Locate every Trypanosoma brucei.
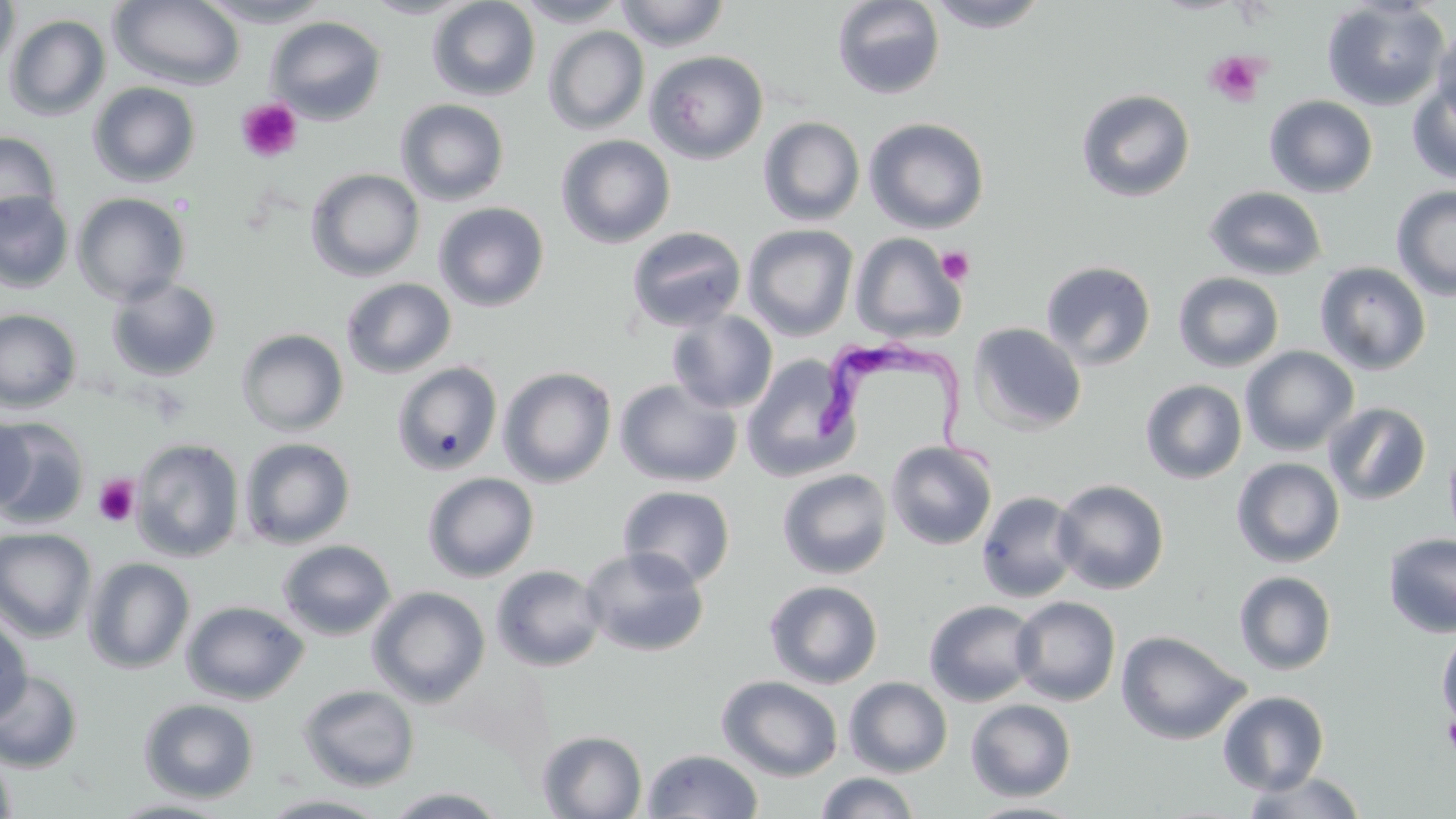
Approximate bounding boxes as named x1/y1/x2/y2 corners in pixels.
Trypanosoma brucei: (x1=814, y1=330, x2=1003, y2=482).

slide-level diagnosis = Trypanosoma brucei
field of view = single
platelet locations = approximate bounding boxes as named x1/y1/x2/y2 corners in pixels: (x1=1204, y1=51, x2=1267, y2=108), (x1=236, y1=98, x2=303, y2=163), (x1=936, y1=246, x2=975, y2=286), (x1=93, y1=474, x2=141, y2=527), (x1=1441, y1=715, x2=1456, y2=758)
uninfected red blood cell locations = approximate bounding boxes as named x1/y1/x2/y2 corners in pixels: (x1=0, y1=0, x2=20, y2=75), (x1=109, y1=0, x2=247, y2=91), (x1=193, y1=0, x2=334, y2=27), (x1=360, y1=0, x2=478, y2=19), (x1=427, y1=0, x2=541, y2=102), (x1=513, y1=0, x2=630, y2=27), (x1=614, y1=0, x2=730, y2=51), (x1=831, y1=0, x2=946, y2=100), (x1=925, y1=0, x2=1052, y2=33), (x1=1321, y1=1, x2=1450, y2=111), (x1=5, y1=14, x2=110, y2=122), (x1=265, y1=16, x2=387, y2=125), (x1=1432, y1=20, x2=1456, y2=128), (x1=543, y1=26, x2=649, y2=135), (x1=645, y1=51, x2=769, y2=165), (x1=1406, y1=80, x2=1456, y2=185), (x1=88, y1=82, x2=201, y2=187), (x1=1075, y1=88, x2=1195, y2=203), (x1=1264, y1=95, x2=1379, y2=198), (x1=395, y1=98, x2=510, y2=206), (x1=758, y1=116, x2=866, y2=226), (x1=864, y1=117, x2=990, y2=233), (x1=0, y1=132, x2=61, y2=231), (x1=556, y1=134, x2=676, y2=248), (x1=306, y1=167, x2=425, y2=282), (x1=1391, y1=185, x2=1456, y2=301), (x1=1203, y1=186, x2=1328, y2=280), (x1=0, y1=191, x2=74, y2=292), (x1=72, y1=192, x2=190, y2=306), (x1=433, y1=201, x2=550, y2=312), (x1=742, y1=224, x2=858, y2=340), (x1=625, y1=225, x2=747, y2=332), (x1=850, y1=232, x2=966, y2=344), (x1=1040, y1=260, x2=1157, y2=370), (x1=1314, y1=261, x2=1431, y2=375), (x1=1174, y1=272, x2=1285, y2=373), (x1=106, y1=277, x2=222, y2=382), (x1=341, y1=277, x2=457, y2=379), (x1=0, y1=309, x2=82, y2=413), (x1=666, y1=310, x2=778, y2=414), (x1=968, y1=322, x2=1087, y2=434), (x1=236, y1=328, x2=349, y2=436), (x1=1239, y1=346, x2=1359, y2=456), (x1=741, y1=354, x2=860, y2=481), (x1=391, y1=361, x2=503, y2=476), (x1=498, y1=366, x2=617, y2=487), (x1=614, y1=378, x2=742, y2=487), (x1=1140, y1=379, x2=1247, y2=484), (x1=1324, y1=402, x2=1432, y2=506), (x1=0, y1=412, x2=34, y2=514), (x1=0, y1=418, x2=91, y2=529), (x1=238, y1=437, x2=356, y2=549), (x1=131, y1=438, x2=245, y2=562), (x1=885, y1=440, x2=998, y2=550), (x1=1231, y1=457, x2=1345, y2=567), (x1=776, y1=468, x2=893, y2=580), (x1=421, y1=472, x2=539, y2=582), (x1=1052, y1=479, x2=1169, y2=594), (x1=618, y1=485, x2=736, y2=588), (x1=976, y1=490, x2=1082, y2=602), (x1=0, y1=527, x2=97, y2=642), (x1=1383, y1=532, x2=1456, y2=638), (x1=277, y1=539, x2=397, y2=641), (x1=581, y1=546, x2=709, y2=658), (x1=83, y1=557, x2=195, y2=674), (x1=491, y1=565, x2=607, y2=672), (x1=1234, y1=570, x2=1337, y2=675), (x1=764, y1=580, x2=884, y2=689), (x1=367, y1=586, x2=490, y2=707), (x1=1011, y1=596, x2=1121, y2=706), (x1=923, y1=599, x2=1040, y2=707), (x1=181, y1=600, x2=309, y2=705), (x1=0, y1=614, x2=32, y2=725), (x1=1436, y1=627, x2=1456, y2=734), (x1=1116, y1=630, x2=1250, y2=745), (x1=0, y1=670, x2=83, y2=773), (x1=717, y1=675, x2=843, y2=782), (x1=844, y1=676, x2=952, y2=778), (x1=297, y1=684, x2=420, y2=792), (x1=1217, y1=690, x2=1330, y2=795), (x1=138, y1=698, x2=260, y2=803), (x1=965, y1=699, x2=1077, y2=802), (x1=537, y1=730, x2=647, y2=819), (x1=0, y1=747, x2=17, y2=819), (x1=641, y1=748, x2=764, y2=819), (x1=1240, y1=771, x2=1369, y2=818), (x1=815, y1=772, x2=922, y2=819), (x1=384, y1=786, x2=509, y2=818), (x1=258, y1=793, x2=392, y2=818), (x1=107, y1=797, x2=235, y2=818), (x1=962, y1=800, x2=1090, y2=819)
modality = optical microscopy
preparation = thin blood smear
image size = 1456×819 pixels
stain = May-Grünwald-Giemsa
magnification = 1000x